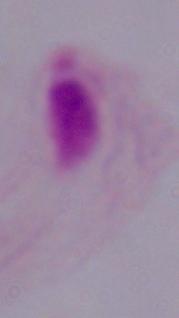
Summary:
  - Identification: trichomonad
  - Modality: micrograph
  - Magnification: 1000x